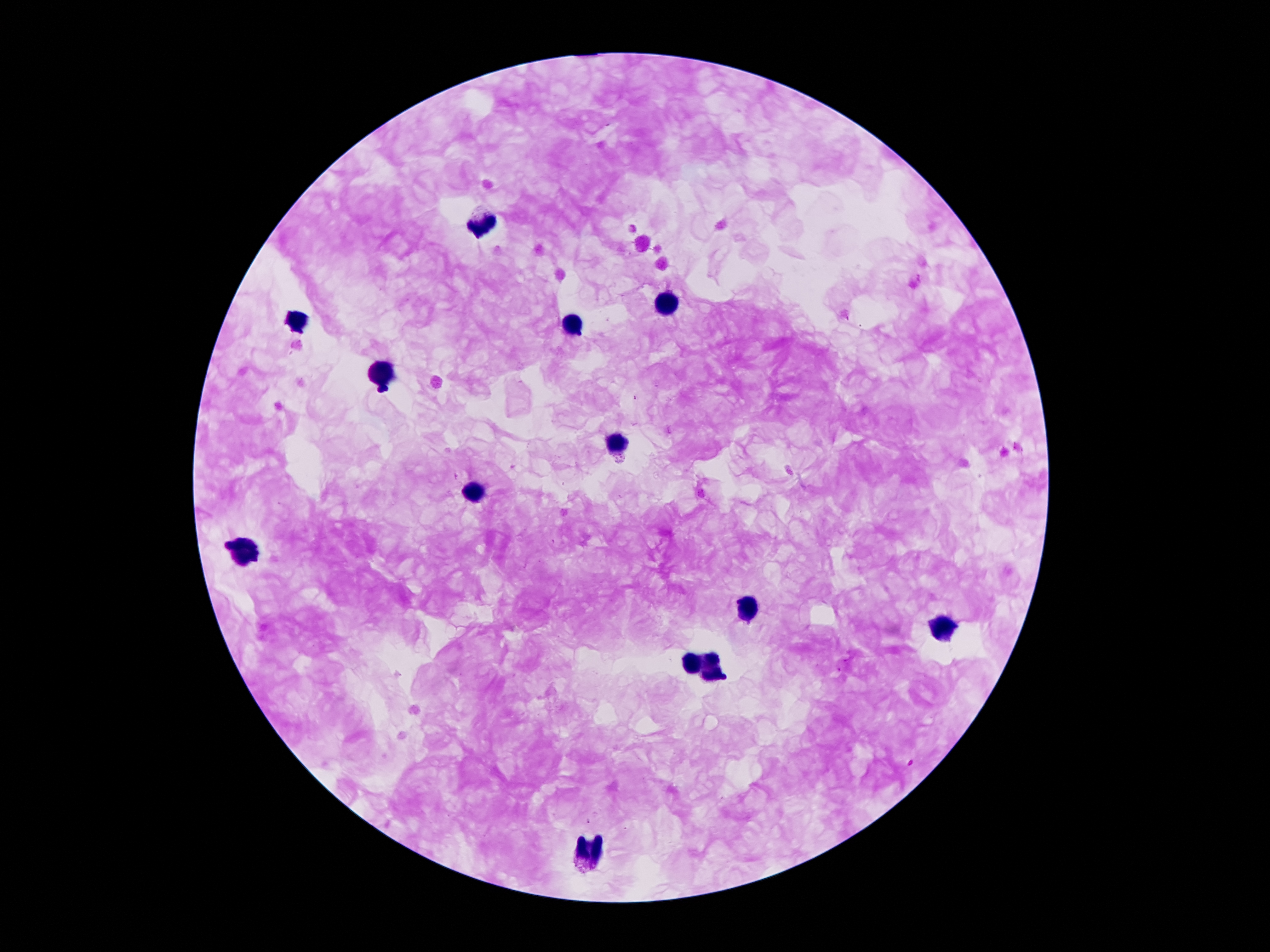

Approximate centers as {x, y} in pixels.
Summary:
  - Leukocyte locations: {484, 222}, {665, 306}, {570, 320}, {295, 322}, {379, 372}, {613, 445}, {469, 496}, {241, 555}, {745, 608}, {941, 626}, {693, 665}, {715, 668}, {591, 849}
  - Malaria parasite locations: {911, 762}, {589, 821}
  - Image size: 1270×952 pixels
  - Stain: Giemsa
  - Preparation: thick peripheral-blood smear
  - Capture: smartphone through the microscope eyepiece
  - Field of view: one from this slide
  - Magnification: 100x
  - Patient malaria status: infected with Plasmodium falciparum